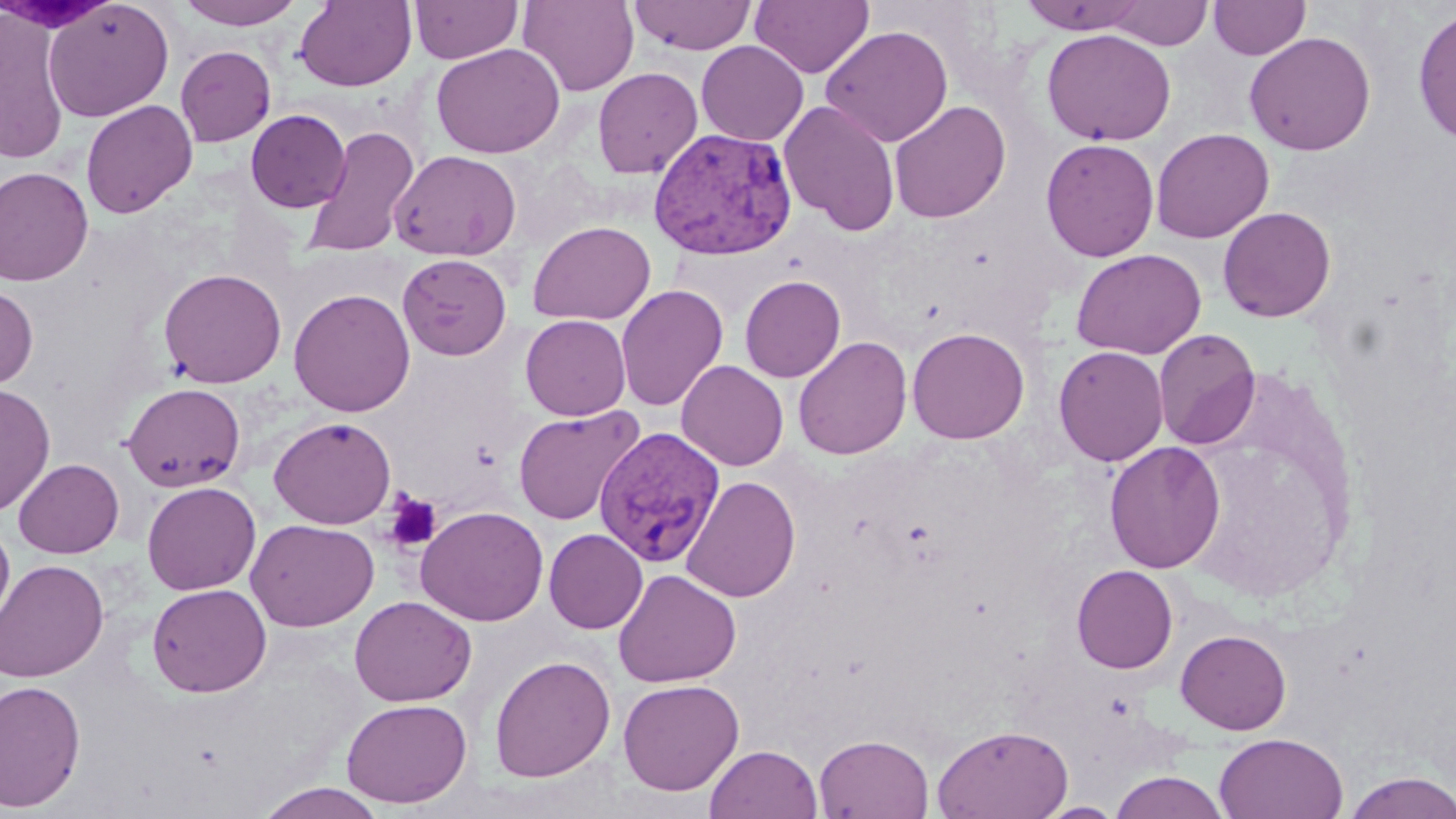 Approximate bounding boxes as (x1, y1, x2, y2) in pixels. Plasmodium vivax-infected red blood cell locations: (648, 126, 798, 261), (594, 426, 727, 567). Platelet locations: (383, 491, 442, 553). Uninfected red blood cell locations: (176, 0, 305, 29), (294, 0, 417, 92), (409, 0, 523, 64), (518, 0, 639, 96), (629, 0, 758, 55), (750, 0, 874, 79), (1018, 0, 1150, 34), (1209, 0, 1311, 60), (44, 1, 174, 121), (1105, 1, 1214, 50), (1413, 6, 1456, 146), (0, 8, 71, 166), (820, 25, 954, 148), (1041, 28, 1177, 146), (1243, 31, 1377, 156), (696, 40, 809, 146), (431, 43, 565, 158), (175, 45, 276, 147), (593, 67, 703, 179), (81, 100, 197, 218), (778, 100, 901, 236), (889, 100, 1011, 223), (245, 109, 350, 212), (301, 124, 420, 260), (1150, 128, 1274, 243), (1040, 138, 1160, 261), (389, 149, 522, 261), (0, 167, 94, 286), (1218, 206, 1336, 322), (528, 220, 656, 325), (1071, 248, 1206, 360), (397, 253, 512, 360), (158, 267, 287, 388), (740, 275, 846, 382), (615, 284, 728, 411), (0, 285, 38, 389), (289, 288, 416, 417), (520, 314, 631, 421), (907, 326, 1029, 444), (1153, 328, 1260, 449), (793, 336, 912, 459), (1053, 345, 1169, 466), (676, 360, 789, 471), (122, 382, 246, 492), (0, 383, 56, 516), (513, 405, 644, 526), (268, 416, 396, 529), (1103, 441, 1226, 573), (13, 458, 124, 558), (681, 475, 801, 602), (142, 481, 261, 595), (416, 505, 548, 626), (245, 518, 379, 632), (0, 521, 15, 634), (544, 528, 647, 633), (0, 559, 108, 683), (1071, 564, 1178, 674), (613, 569, 741, 688), (146, 583, 271, 697), (350, 595, 476, 707), (1175, 629, 1292, 734), (489, 655, 616, 783), (0, 679, 86, 812), (618, 679, 744, 795), (341, 697, 472, 807), (931, 723, 1073, 818), (1214, 732, 1348, 819), (814, 733, 934, 818), (704, 744, 823, 819), (1109, 770, 1231, 819), (1342, 771, 1456, 819), (254, 782, 389, 818), (1036, 801, 1125, 818). Slide-level diagnosis: Plasmodium vivax. Optical microscopy. Image is 1456×819 pixels. One field of a larger specimen. May-Grünwald-Giemsa stain. Thin blood film. 1000x magnification.